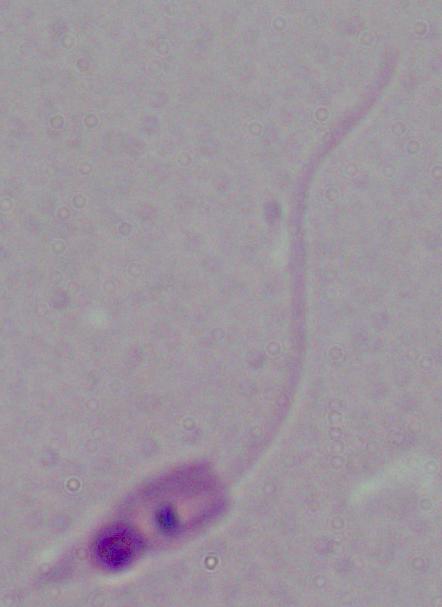

magnification: 1000x
identification: Leishmania
modality: micrograph